Locate every white blood cell.
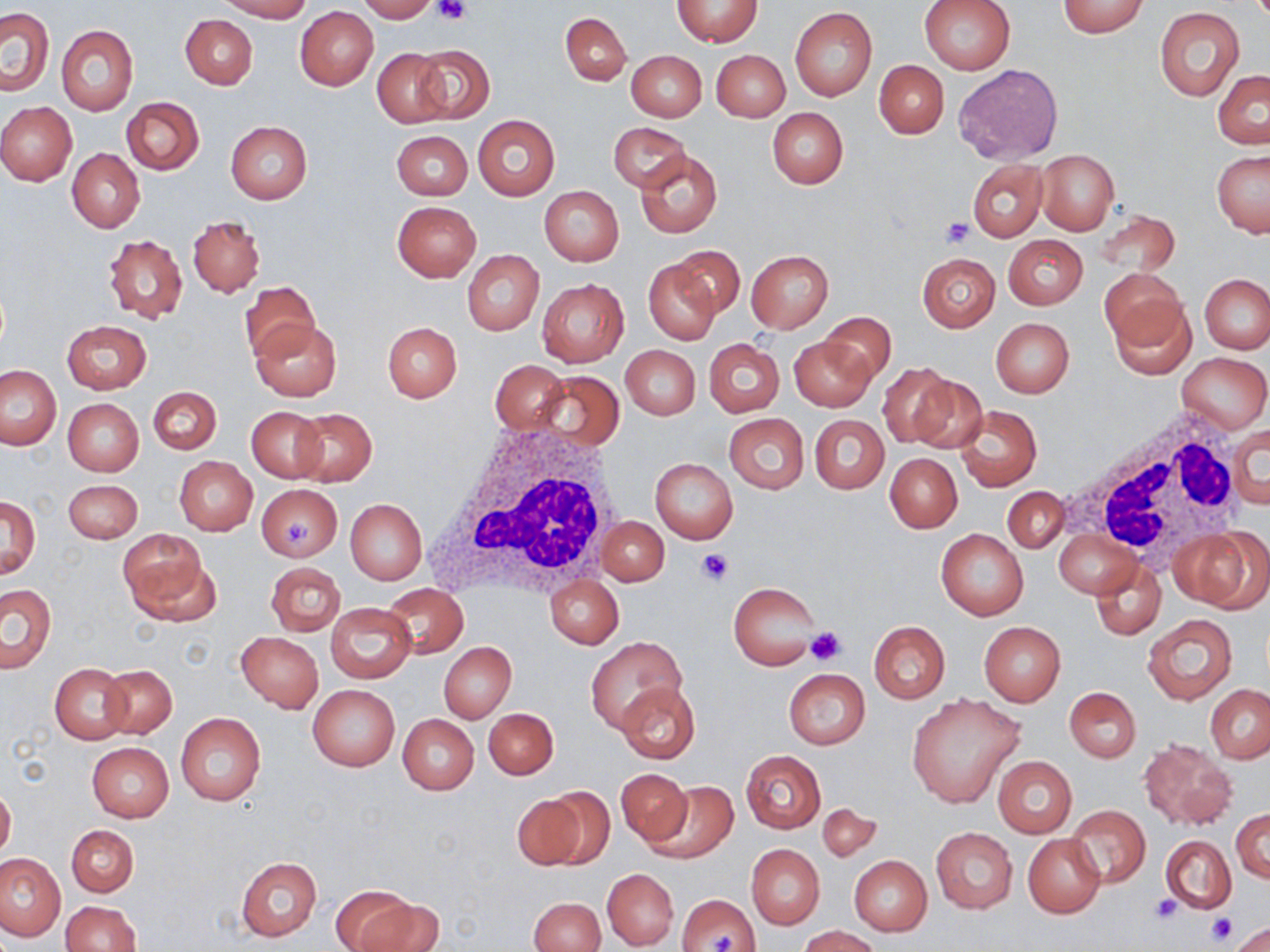

Approximate bounding boxes as (x1,y1)-(x2,y2) corner pairs in pixels.
White blood cells: (1069,405)-(1246,573), (427,418)-(629,594).

Platelet locations: (434,0)-(471,25), (940,218)-(972,247), (285,518)-(316,546), (696,549)-(734,585), (804,625)-(848,665), (1150,892)-(1182,923), (1205,914)-(1237,946), (706,932)-(736,952). Uninfected red blood cell locations: (217,0)-(310,21), (357,0)-(436,22), (918,0)-(1016,75), (672,1)-(761,47), (1057,1)-(1149,37), (1,6)-(55,96), (295,6)-(378,90), (790,7)-(877,100), (1154,7)-(1244,100), (560,12)-(631,86), (180,16)-(257,89), (57,24)-(138,115), (412,44)-(494,123), (372,48)-(451,128), (626,50)-(707,122), (712,50)-(789,121), (874,59)-(948,138), (953,64)-(1064,165), (1212,69)-(1270,149), (121,97)-(204,175), (0,102)-(77,186), (767,108)-(848,189), (473,115)-(560,200), (225,121)-(312,203), (608,122)-(691,191), (391,130)-(472,200), (67,149)-(144,232), (636,150)-(722,238), (1035,150)-(1120,233), (1213,150)-(1269,237), (968,160)-(1048,241), (539,186)-(624,265), (391,201)-(480,281), (1095,208)-(1181,276), (188,216)-(264,297), (103,234)-(188,324), (1004,235)-(1087,309), (670,246)-(745,319), (463,250)-(544,335), (746,250)-(834,333), (917,252)-(999,331), (644,258)-(719,344), (1101,268)-(1189,351), (1200,274)-(1270,352), (537,279)-(628,366), (240,282)-(320,361), (1108,296)-(1199,381), (820,311)-(896,385), (990,317)-(1075,397), (61,319)-(151,394), (251,319)-(342,402), (382,321)-(462,403), (789,337)-(872,412), (703,339)-(784,416), (621,345)-(700,419), (1178,352)-(1268,434), (490,360)-(568,437), (0,364)-(62,450), (877,365)-(959,448), (536,372)-(624,452), (908,374)-(988,454), (150,386)-(222,454), (62,398)-(143,476), (955,405)-(1041,492), (247,407)-(327,482), (291,408)-(377,485), (724,413)-(809,493), (811,415)-(889,494), (1229,423)-(1268,513), (886,454)-(961,533), (174,457)-(256,535), (650,458)-(737,543), (63,480)-(142,543), (257,484)-(343,562), (1002,487)-(1068,554), (1,496)-(40,578), (346,499)-(426,584), (599,517)-(668,586), (1175,527)-(1266,610), (936,528)-(1028,620), (118,529)-(208,619), (1056,529)-(1143,598), (1091,560)-(1165,640), (265,563)-(344,636), (545,576)-(622,648), (1,582)-(56,673), (729,583)-(819,671), (382,584)-(468,659), (326,603)-(416,683), (1142,614)-(1237,705), (868,621)-(949,703), (979,622)-(1065,705), (236,632)-(324,711), (586,638)-(684,733), (440,642)-(516,723), (51,663)-(131,743), (100,664)-(177,738), (784,669)-(869,749), (615,681)-(701,766), (308,685)-(399,770), (1205,685)-(1270,763), (1065,688)-(1141,762), (907,694)-(1024,809), (483,707)-(558,780), (177,713)-(266,805), (398,714)-(479,795), (1138,738)-(1237,830), (87,742)-(173,822), (741,750)-(826,832), (993,756)-(1077,836), (615,767)-(693,847), (646,783)-(737,864), (0,786)-(15,860), (538,786)-(615,869), (512,793)-(584,869), (817,804)-(882,862), (1066,804)-(1150,888), (1232,810)-(1270,882), (66,824)-(138,897), (932,828)-(1017,913), (1023,835)-(1105,917), (1161,835)-(1236,913), (747,845)-(825,928), (0,853)-(67,941), (849,855)-(932,936), (236,856)-(322,941), (602,869)-(678,949), (329,886)-(425,951), (676,893)-(761,952), (529,898)-(605,952), (60,900)-(141,952), (1230,921)-(1270,952), (798,925)-(884,951). Slide-level diagnosis: negative for blood parasites. One field of a larger specimen. Image is 1270×952 pixels. Thin blood smear. May-Grünwald-Giemsa-stained preparation. Light microscopy. 1000x magnification.